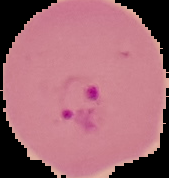
From a thin blood film. Image is 169×178 pixels. Malaria status: parasitized. Segmented cell region on a black background.